Describe the morphology of the red blood cells.
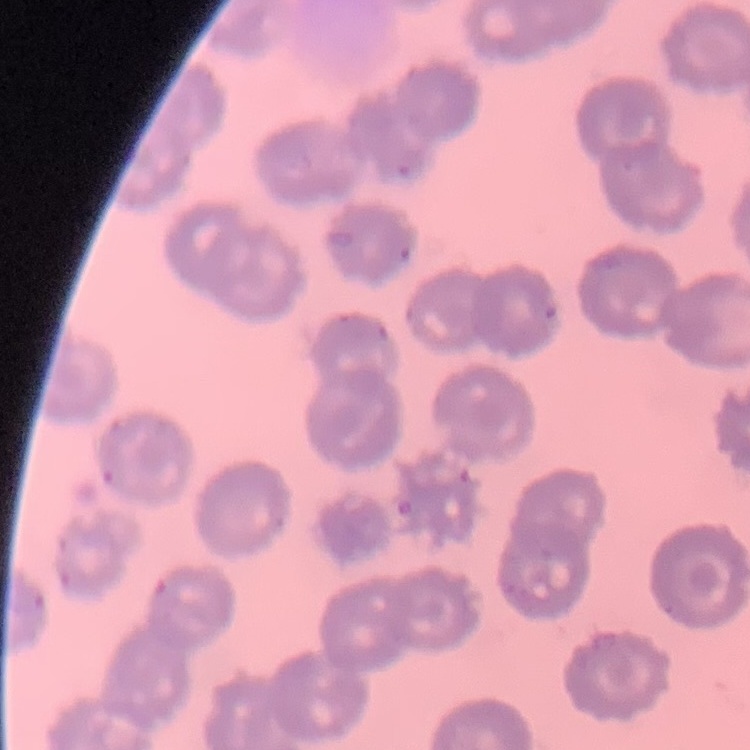
They show no rouleaux formation.

Summary:
  - Stain: Field's or Giemsa
  - Image type: one tile cut from a larger photomicrograph
  - Preparation: thin blood film